State the blood parasite species.
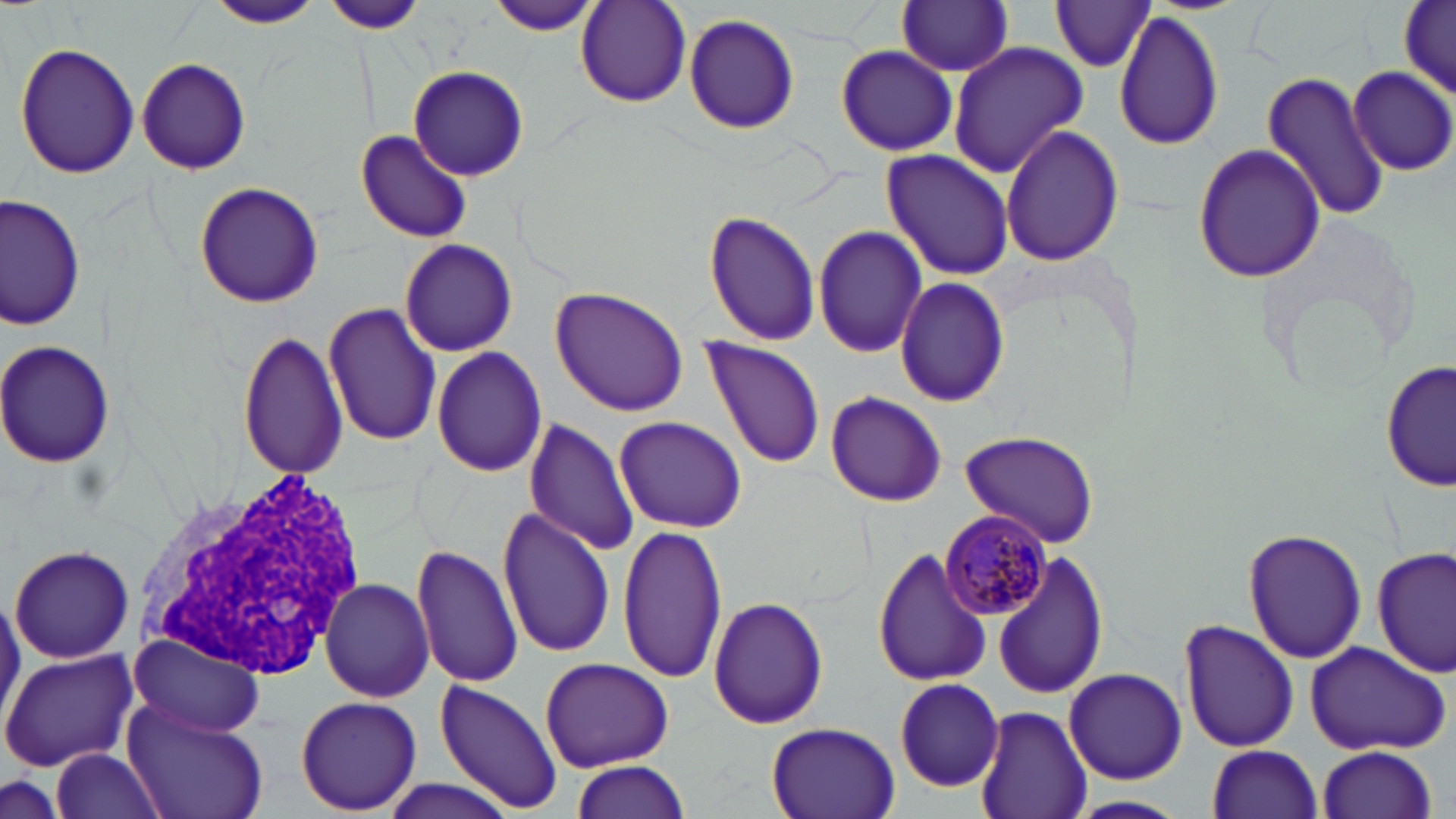

Plasmodium malariae.

Summary:
  - Coordinate format: approximate bounding boxes as named x1/y1/x2/y2 corners in pixels
  - White blood cell locations: (x1=125, y1=463, x2=372, y2=687)
  - Uninfected red blood cell locations: (x1=207, y1=0, x2=323, y2=30), (x1=327, y1=0, x2=424, y2=34), (x1=484, y1=1, x2=604, y2=37), (x1=896, y1=1, x2=1015, y2=76), (x1=1049, y1=1, x2=1156, y2=74), (x1=576, y1=2, x2=691, y2=106), (x1=1398, y1=2, x2=1455, y2=100), (x1=683, y1=12, x2=802, y2=135), (x1=1113, y1=12, x2=1225, y2=150), (x1=947, y1=41, x2=1091, y2=180), (x1=14, y1=42, x2=140, y2=181), (x1=836, y1=43, x2=960, y2=160), (x1=134, y1=58, x2=252, y2=175), (x1=407, y1=66, x2=528, y2=179), (x1=1350, y1=66, x2=1454, y2=174), (x1=1258, y1=69, x2=1391, y2=224), (x1=1000, y1=125, x2=1123, y2=266), (x1=355, y1=130, x2=471, y2=242), (x1=1193, y1=141, x2=1325, y2=286), (x1=881, y1=150, x2=1015, y2=281), (x1=194, y1=181, x2=325, y2=307), (x1=1, y1=193, x2=83, y2=330), (x1=703, y1=208, x2=822, y2=347), (x1=811, y1=225, x2=927, y2=359), (x1=397, y1=238, x2=517, y2=357), (x1=896, y1=278, x2=1011, y2=406), (x1=550, y1=287, x2=689, y2=416), (x1=324, y1=302, x2=443, y2=448), (x1=236, y1=329, x2=349, y2=480), (x1=0, y1=339, x2=116, y2=468), (x1=702, y1=339, x2=826, y2=468), (x1=432, y1=347, x2=547, y2=478), (x1=1382, y1=357, x2=1454, y2=495), (x1=825, y1=391, x2=946, y2=507), (x1=614, y1=417, x2=746, y2=531), (x1=524, y1=418, x2=638, y2=555), (x1=958, y1=429, x2=1100, y2=549), (x1=496, y1=506, x2=614, y2=660), (x1=618, y1=523, x2=725, y2=683), (x1=1243, y1=529, x2=1366, y2=665), (x1=410, y1=542, x2=523, y2=690), (x1=9, y1=543, x2=135, y2=665), (x1=873, y1=546, x2=993, y2=688), (x1=1373, y1=547, x2=1454, y2=682), (x1=993, y1=554, x2=1108, y2=703), (x1=318, y1=579, x2=435, y2=702), (x1=708, y1=596, x2=830, y2=731), (x1=1179, y1=619, x2=1301, y2=754), (x1=127, y1=632, x2=266, y2=739), (x1=1301, y1=640, x2=1451, y2=755), (x1=0, y1=648, x2=140, y2=772), (x1=537, y1=657, x2=676, y2=770), (x1=1062, y1=669, x2=1189, y2=785), (x1=895, y1=679, x2=1004, y2=790), (x1=435, y1=680, x2=562, y2=813), (x1=295, y1=694, x2=421, y2=815), (x1=122, y1=698, x2=267, y2=819), (x1=973, y1=705, x2=1091, y2=819), (x1=764, y1=723, x2=901, y2=819), (x1=1207, y1=744, x2=1323, y2=819), (x1=1318, y1=745, x2=1437, y2=819), (x1=46, y1=749, x2=169, y2=819), (x1=571, y1=760, x2=690, y2=817), (x1=1, y1=775, x2=69, y2=819), (x1=374, y1=777, x2=523, y2=819), (x1=1068, y1=795, x2=1190, y2=819)
  - Plasmodium malariae-infected red blood cell locations: (x1=940, y1=510, x2=1054, y2=620)
  - Modality: optical microscopy
  - Stain: May-Grünwald-Giemsa
  - Image size: 1456×819 pixels
  - Magnification: 1000x
  - Field of view: one of a larger specimen
  - Preparation: thin blood film